Report the malaria status of this cell.
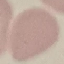

It is uninfected.

Summary:
  - Preparation: thin blood film
  - Image type: cell patch, automatically extracted from a larger field of view and resized to 64 × 64 pixels
  - Stain: Giemsa
  - Capture: smartphone camera at the microscope eyepiece